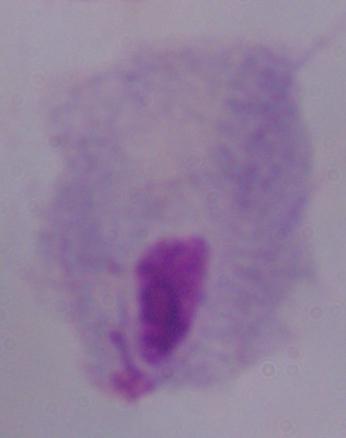

Photomicrograph. A trichomonad is shown. Captured at 1000x magnification.